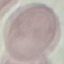

{
  "malaria_status": "uninfected",
  "stain": "Giemsa",
  "image_type": "cell patch, automatically extracted from a larger field of view and resized to 64 × 64 pixels",
  "capture": "smartphone camera at the microscope eyepiece",
  "preparation": "thin smear"
}